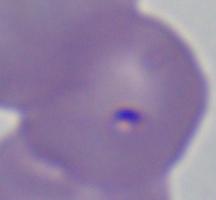

identification = Babesia
magnification = 1000x
modality = micrograph